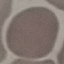
Summary:
  - Malaria status: uninfected
  - Preparation: thin smear
  - Stain: Giemsa
  - Capture: smartphone camera at the microscope eyepiece
  - Image type: automatically extracted cell patch, resized to 64 × 64 pixels